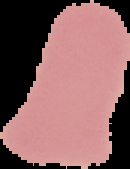

Summary:
  - Image type: cell region segmented out of the field of view; surrounding area masked to black
  - Image size: 130×169 pixels
  - Preparation: thin blood film
  - Result: no malaria parasites seen